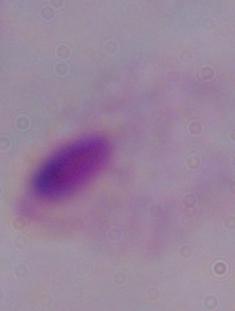

Captured at 1000x magnification. Photomicrograph. A trichomonad is shown.